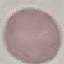
malaria status = uninfected
capture = smartphone camera at the microscope eyepiece
preparation = thin blood film
stain = Giemsa
image type = automatically extracted cell patch, resized to 64 × 64 pixels